Assess this cell for malaria.
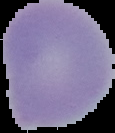

Uninfected.

preparation = thin blood film
image size = 115×133 pixels
image type = segmented cell region on a black background